Assess the morphology of the erythrocytes.
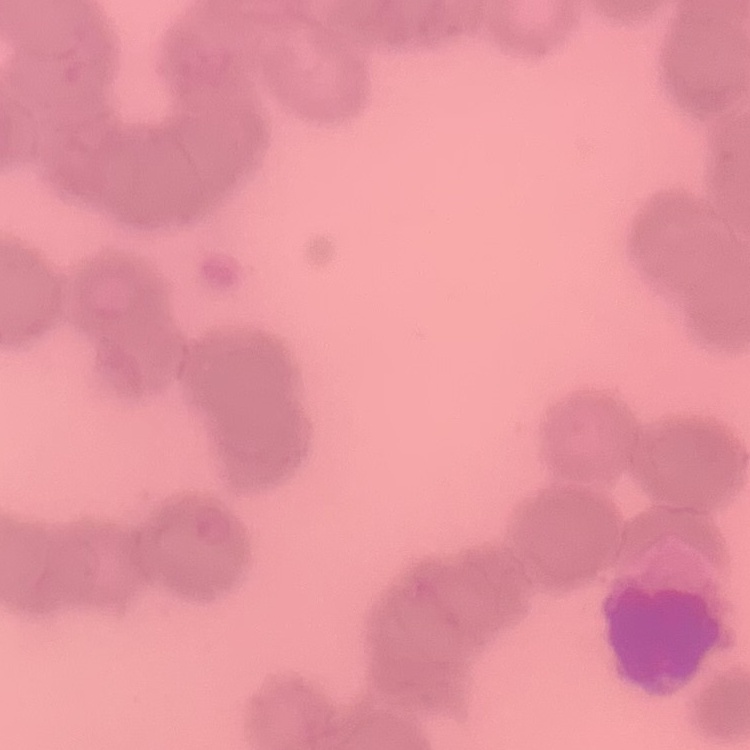
They show rouleaux formation.

{
  "image_type": "square crop of a larger photomicrograph",
  "preparation": "thin blood smear",
  "stain": "Field's or Giemsa"
}